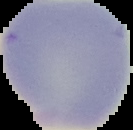
Result: no Plasmodium parasites seen. Image is 133×130 pixels. From a thin blood film. Cell region segmented out of the field of view; the surrounding area is masked to black.